Identify the parasite.
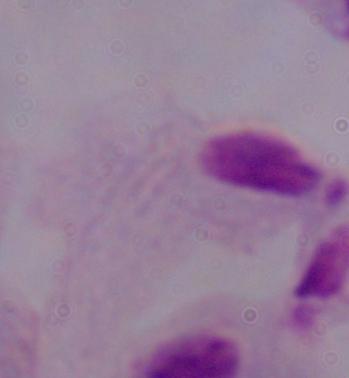
This is a trichomonad.

magnification = 1000x
modality = micrograph